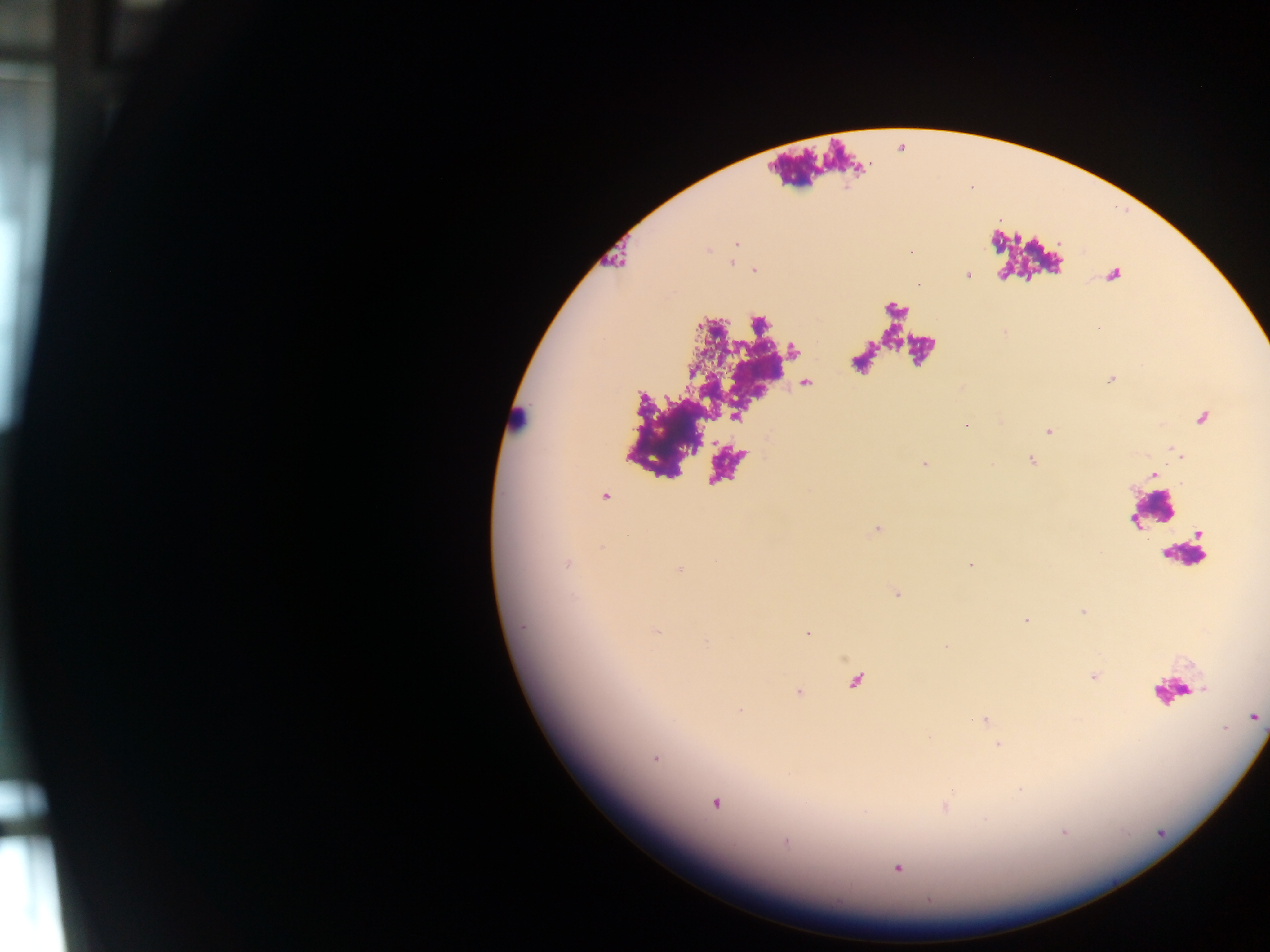
Approximate centers as [x, y] in pixels.
Summary:
  - Leukocyte locations: [516, 416], [1150, 509], [1173, 690]
  - Malaria parasite locations: [736, 244], [732, 263], [754, 271], [968, 275], [966, 425], [1048, 431], [1031, 460], [924, 464], [605, 496], [568, 563], [970, 564], [679, 570], [897, 594], [1083, 611], [1026, 620], [522, 626], [657, 632], [807, 634], [706, 641], [1093, 676], [740, 711], [1254, 717], [986, 721], [998, 745], [655, 759], [715, 803], [946, 807], [1063, 832], [785, 841], [898, 868]
  - Preparation: thick blood film
  - Field of view: single
  - Capture: mobile-phone photograph through a microscope
  - Image size: 1270×952 pixels
  - Country: Ghana